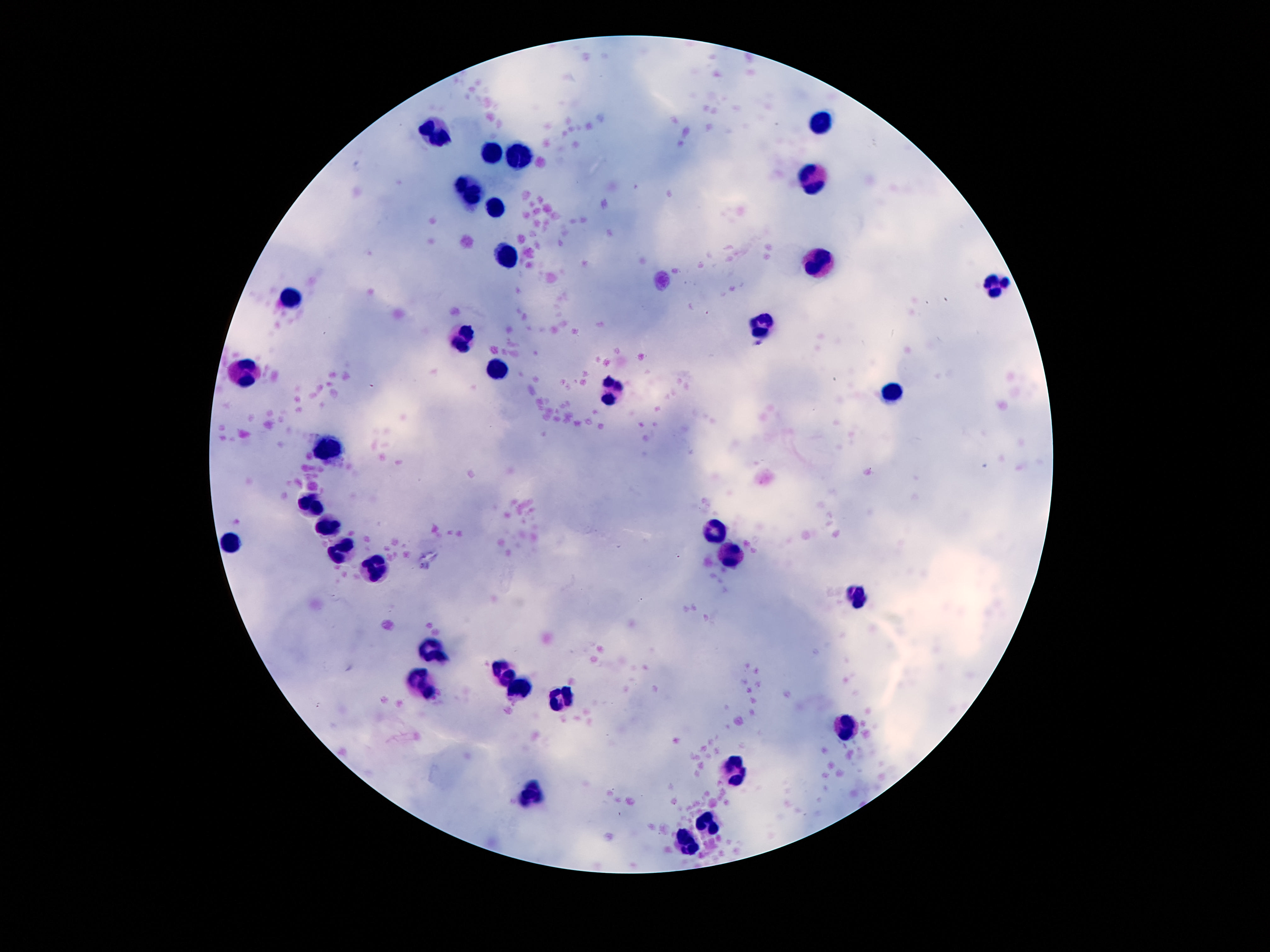
Approximate object centers, in pixels from the top-left corner. Leukocyte locations: (x=822, y=123), (x=437, y=132), (x=493, y=153), (x=520, y=158), (x=810, y=180), (x=468, y=186), (x=493, y=207), (x=506, y=255), (x=817, y=263), (x=995, y=286), (x=291, y=298), (x=762, y=326), (x=464, y=338), (x=244, y=372), (x=498, y=372), (x=612, y=392), (x=891, y=392), (x=330, y=451), (x=313, y=506), (x=329, y=525), (x=717, y=532), (x=233, y=542), (x=341, y=552), (x=730, y=559), (x=372, y=567), (x=860, y=596), (x=430, y=652), (x=503, y=674), (x=419, y=679), (x=524, y=689), (x=566, y=698), (x=851, y=729), (x=732, y=771), (x=530, y=798), (x=708, y=822), (x=688, y=845). Thick blood smear. Giemsa-stained preparation. Smartphone photograph taken through the microscope eyepiece. Patient malaria status: uninfected. Single field of view. Image is 1270×952 pixels. 100x magnification.